Give a bounding box for every leukocyte visible.
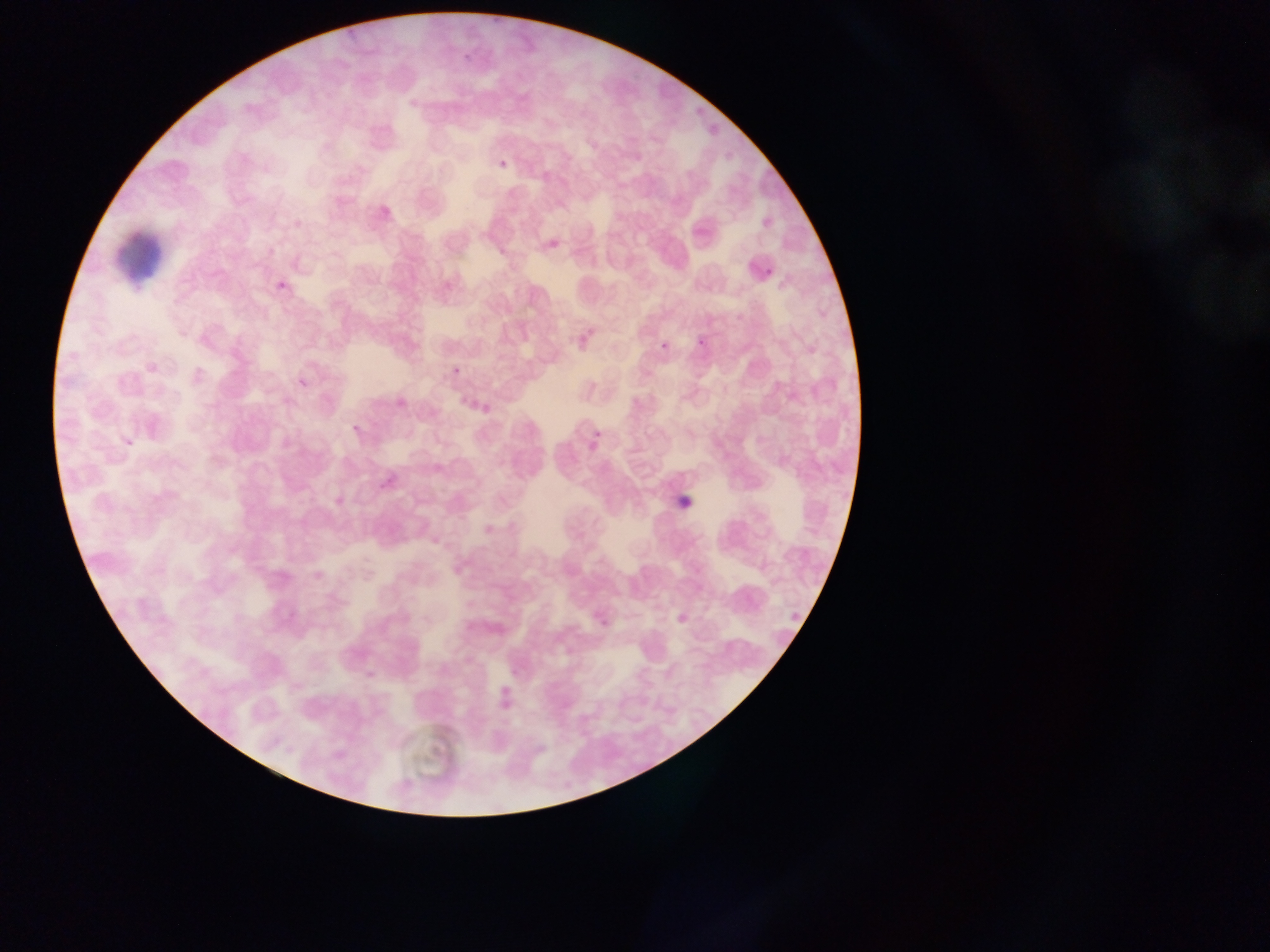
No leukocytes observed.

artifact (stain precipitate or debris) locations = approximate bounding boxes as left top right bottom in pixels: 111 220 166 279
capture = mobile-phone photograph through a microscope
field of view = single
preparation = thin blood film
image size = 1270×952 pixels
country = Ghana
malaria parasite locations = approximate bounding boxes as left top right bottom in pixels: 461 51 475 65; 494 152 511 167; 761 263 778 281; 273 265 290 292; 693 332 713 354; 657 333 671 349; 577 336 585 351; 291 363 312 393; 452 366 462 377; 586 413 610 445; 350 422 363 435; 673 490 700 518; 597 603 618 629; 672 605 698 634; 495 688 508 711